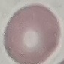

malaria status = uninfected
capture = smartphone camera at the microscope eyepiece
preparation = thin blood smear
image type = cell patch, automatically extracted from a larger field of view and resized to 64 × 64 pixels
stain = Giemsa